Locate every Plasmodium falciparum-infected red blood cell.
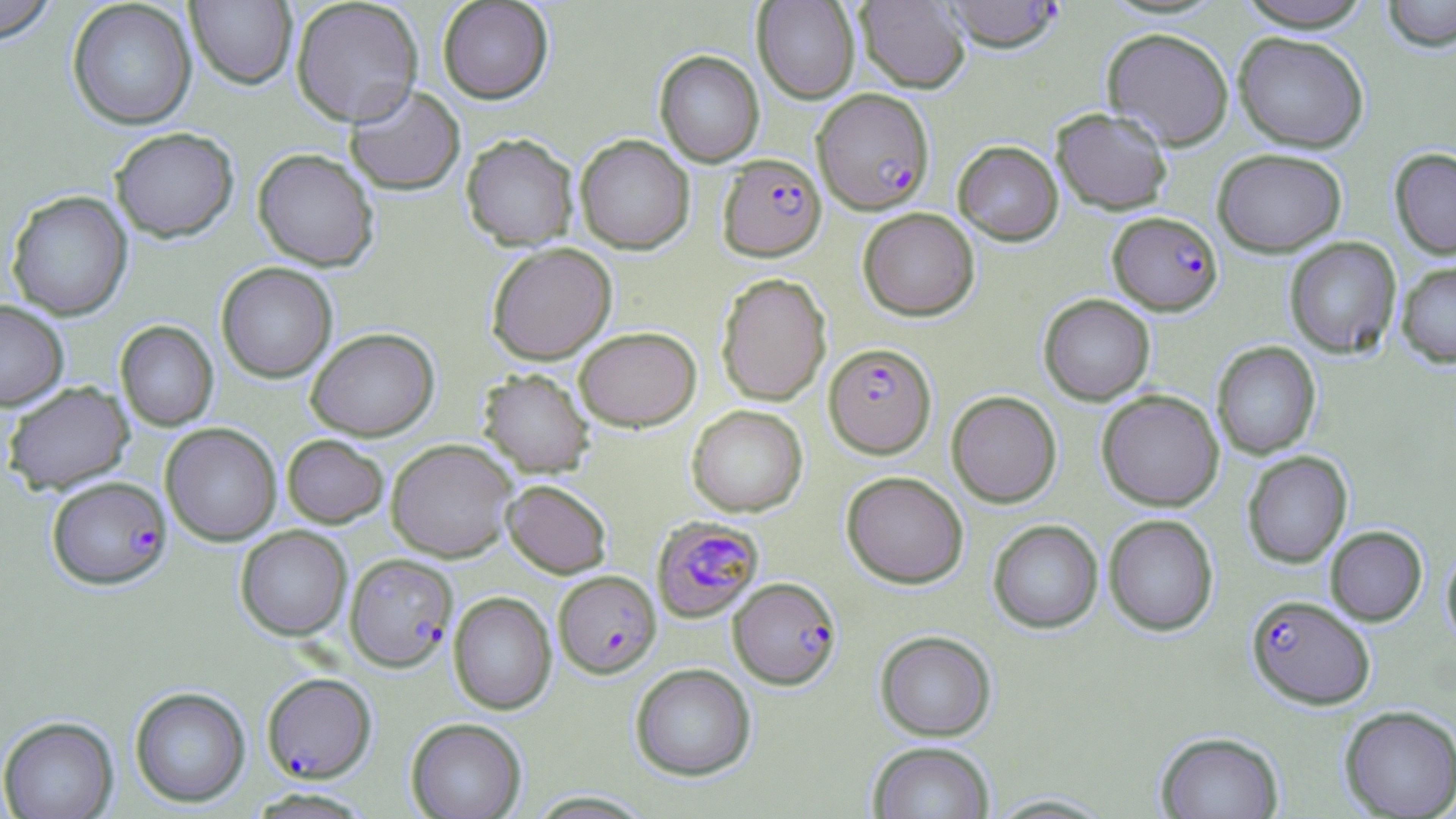
Approximate bounding boxes as (x1,y1)-(x2,y2) corner pairs in pixels.
Plasmodium falciparum-infected red blood cells: (941,0)-(1064,52), (813,88)-(934,214), (718,154)-(826,261), (1108,211)-(1223,315), (825,342)-(936,457), (47,476)-(172,589), (651,516)-(764,622), (345,553)-(458,672), (553,570)-(661,677), (728,577)-(841,689), (1247,594)-(1375,709), (262,672)-(376,782).

Uninfected red blood cell locations: (0,0)-(58,44), (291,0)-(424,126), (438,0)-(554,103), (752,0)-(859,103), (1236,0)-(1375,31), (1382,0)-(1456,51), (67,1)-(197,130), (186,1)-(297,89), (856,1)-(970,94), (1102,27)-(1234,149), (1233,32)-(1369,152), (654,50)-(764,166), (344,85)-(466,196), (1051,107)-(1173,215), (109,127)-(239,242), (461,133)-(579,250), (575,134)-(695,254), (953,140)-(1063,245), (1389,147)-(1456,260), (253,148)-(379,271), (1212,148)-(1347,256), (6,190)-(132,320), (857,207)-(980,321), (1284,237)-(1402,359), (486,242)-(617,364), (1396,260)-(1456,368), (216,262)-(337,383), (716,272)-(831,406), (1039,294)-(1155,405), (0,300)-(68,410), (115,321)-(218,431), (574,326)-(701,431), (306,327)-(439,440), (1212,341)-(1321,459), (478,368)-(594,477), (3,382)-(134,494), (1096,389)-(1224,511), (946,390)-(1062,507), (686,405)-(807,517), (160,423)-(282,546), (282,434)-(389,528), (386,438)-(518,562), (1242,451)-(1352,567), (841,471)-(968,588), (501,479)-(612,578), (1103,514)-(1219,636), (988,519)-(1103,633), (235,525)-(352,640), (1325,525)-(1427,626), (1441,545)-(1456,649), (448,591)-(556,714), (875,630)-(996,741), (630,663)-(756,781), (130,686)-(250,807), (1339,705)-(1456,818), (1,716)-(118,819), (406,717)-(527,819), (1156,730)-(1284,818), (867,741)-(995,819), (246,788)-(376,818), (984,793)-(1118,817). Slide-level diagnosis: Plasmodium falciparum. Captured at 1000x magnification. May-Grünwald-Giemsa-stained preparation. One field of a larger specimen. Image is 1456×819 pixels. Thin blood smear. Optical microscopy.